Assess this cell for malaria.
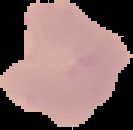
It is parasitized.

Summary:
  - Preparation: thin blood smear
  - Image size: 133×130 pixels
  - Image type: cell region segmented out of the field of view; surrounding area masked to black